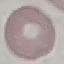

Summary:
  - Result: no malaria parasites detected
  - Image type: automatically extracted cell patch, resized to 64 × 64 pixels
  - Preparation: thin blood smear
  - Capture: smartphone camera at the microscope eyepiece
  - Stain: Giemsa